Name the parasite shown.
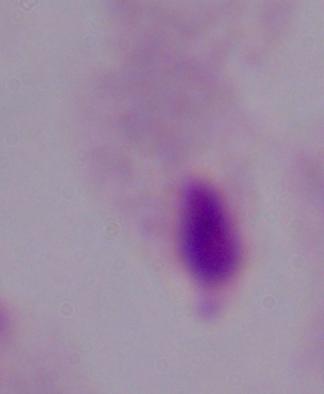
This is a trichomonad.

Summary:
  - Magnification: 1000x
  - Modality: micrograph